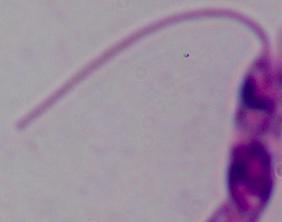
Summary:
  - Magnification: 1000x
  - Modality: micrograph
  - Identification: Leishmania